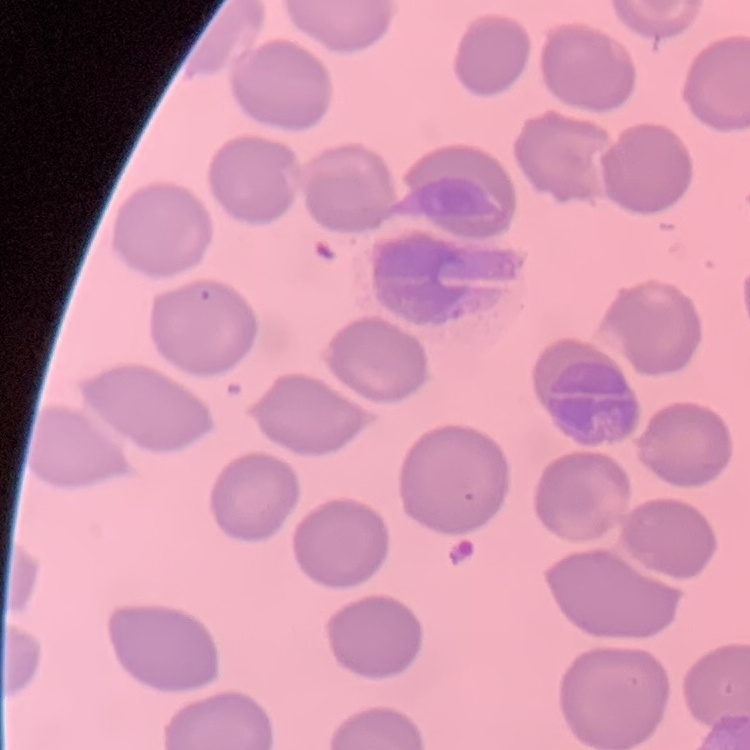

red blood cell morphology = no rouleaux formation
stain = Field's or Giemsa
preparation = thin blood film
image type = square crop of a larger photomicrograph